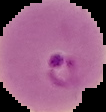 The area outside the segmented cell region is set to black. Result: Plasmodium parasites detected. Image is 106×112 pixels. From a thin blood film.